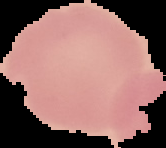
Summary:
  - Preparation: thin blood smear
  - Image size: 166×148 pixels
  - Malaria status: uninfected
  - Image type: segmented cell region on a black background